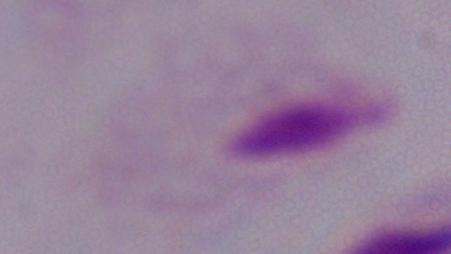

Summary:
  - Magnification: 1000x
  - Modality: micrograph
  - Identification: trichomonad